Comment on the morphology of the red blood cells.
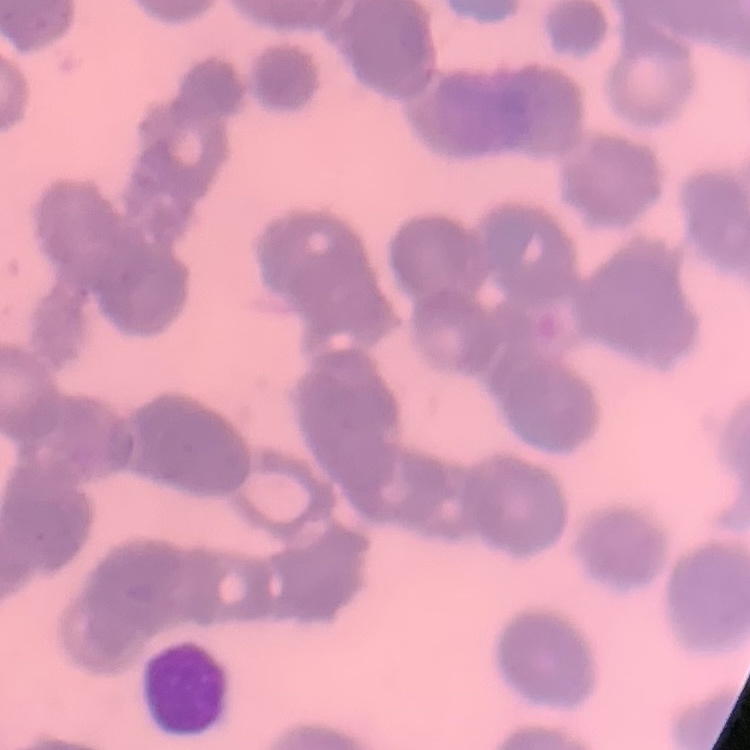

Rouleaux formation.

Summary:
  - Preparation: thin peripheral smear
  - Image type: one tile cut from a larger photomicrograph
  - Stain: Field's or Giemsa